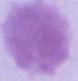

Summary:
  - Identification: erythrocyte
  - Modality: photomicrograph
  - Magnification: 1000x